Report the malaria status of this cell.
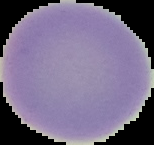

It is uninfected.

Cell region segmented out of the field of view; the surrounding area is masked to black. Image is 154×145 pixels. From a thin blood smear.